Point out each Plasmodium parasite and each leukocyte.
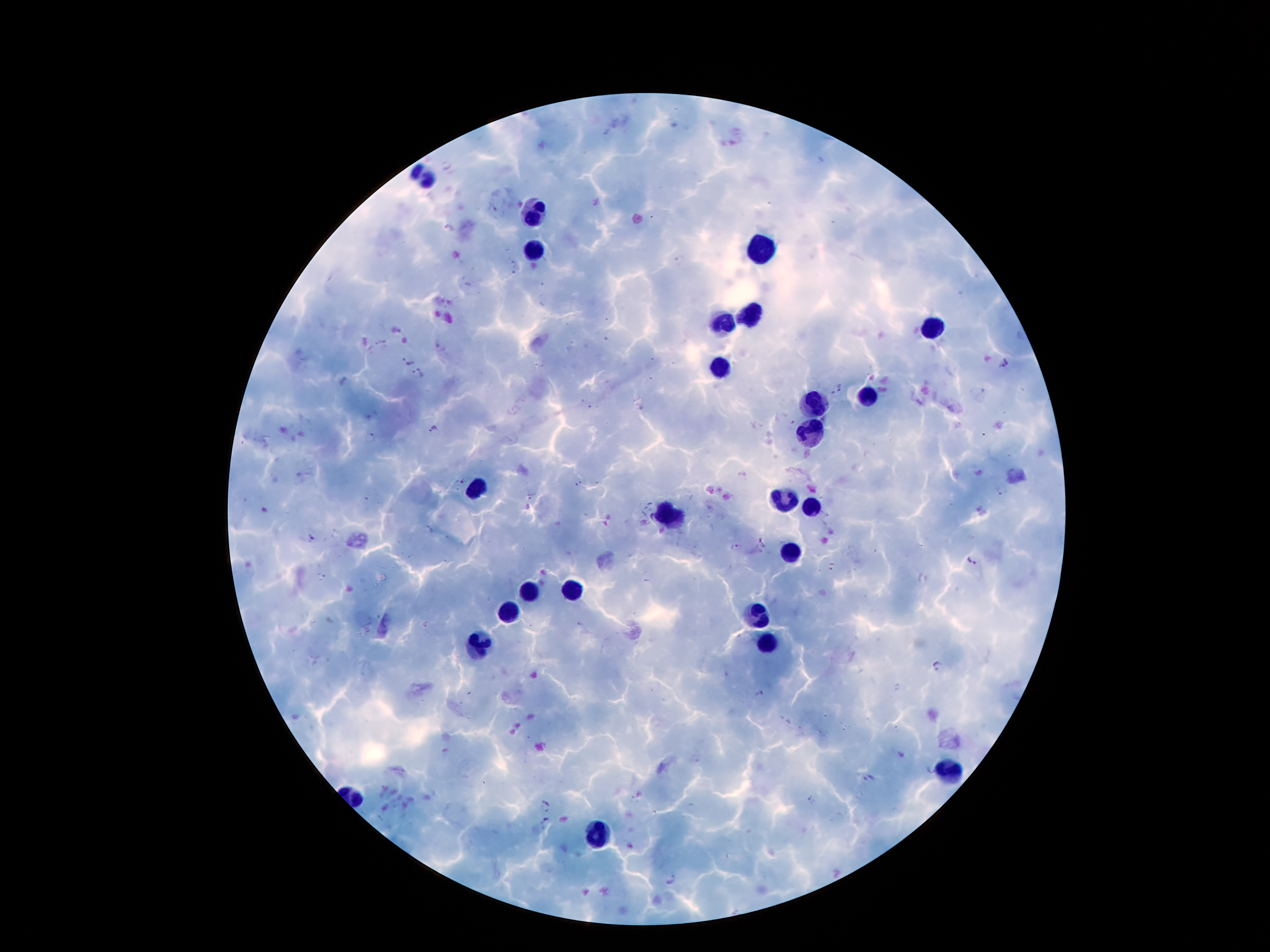
Approximate centers as [x, y] in pixels.
Plasmodium parasites: [406, 363], [1002, 363], [419, 373], [838, 390], [435, 428], [370, 438], [579, 483], [999, 493], [532, 495], [313, 538], [762, 542], [735, 546], [974, 561], [321, 576], [940, 666], [759, 695], [929, 770], [869, 777], [811, 799], [548, 801], [547, 820], [671, 881].
Leukocytes: [423, 179], [530, 213], [535, 248], [759, 250], [749, 315], [723, 324], [931, 327], [720, 370], [870, 398], [817, 404], [812, 432], [478, 487], [782, 500], [812, 505], [672, 516], [791, 553], [576, 589], [529, 592], [509, 612], [758, 615], [479, 643], [768, 643], [949, 770], [596, 834].

preparation = thick peripheral-blood smear
stain = Giemsa
field of view = one from this slide
magnification = 100x
patient malaria status = infected with Plasmodium falciparum
capture = smartphone camera through the microscope eyepiece
image size = 1270×952 pixels